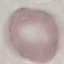
Summary:
  - Result: no malaria parasites seen
  - Image type: cell patch, automatically extracted from a larger field of view and resized to 64 × 64 pixels
  - Stain: Giemsa
  - Capture: smartphone through the microscope eyepiece
  - Preparation: thin blood smear